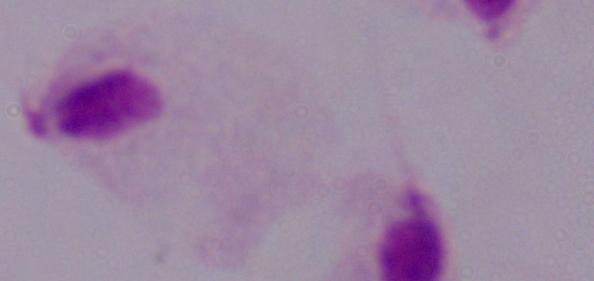

magnification = 1000x
modality = photomicrograph
identification = trichomonad